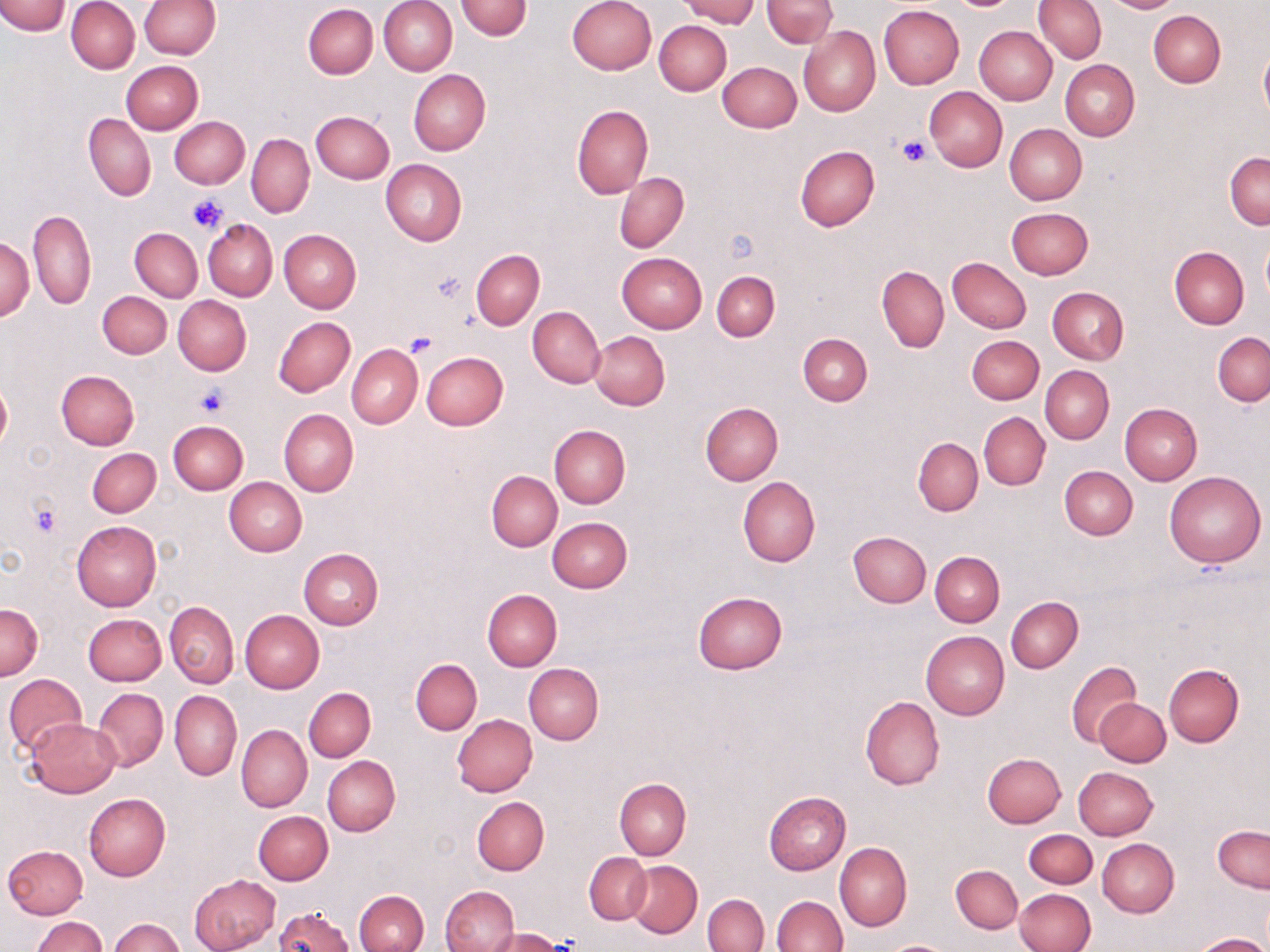
slide-level diagnosis = no evidence of blood parasites
stain = May-Grünwald-Giemsa
uninfected red blood cell locations = approximate bounding boxes as (x1, y1, x2, y2) in pixels: (67, 0, 139, 74), (138, 0, 219, 58), (380, 0, 457, 75), (567, 0, 656, 75), (680, 0, 758, 26), (761, 0, 837, 48), (1034, 0, 1107, 63), (1100, 0, 1183, 13), (0, 1, 70, 36), (456, 1, 532, 40), (303, 4, 378, 79), (878, 5, 964, 88), (1148, 11, 1225, 88), (654, 20, 731, 95), (974, 25, 1057, 104), (798, 26, 879, 116), (1259, 44, 1270, 122), (1060, 59, 1139, 141), (121, 61, 202, 135), (718, 61, 801, 133), (408, 69, 490, 155), (924, 86, 1007, 171), (573, 105, 653, 198), (311, 111, 394, 183), (83, 112, 156, 201), (170, 116, 249, 189), (1005, 123, 1087, 205), (247, 134, 315, 219), (795, 146, 879, 231), (1225, 151, 1270, 228), (380, 159, 467, 246), (615, 173, 689, 253), (1006, 207, 1093, 280), (28, 208, 97, 309), (203, 219, 278, 301), (130, 228, 202, 302), (279, 229, 361, 313), (1261, 236, 1270, 303), (1, 238, 34, 321), (1170, 246, 1249, 328), (472, 250, 544, 330), (616, 252, 708, 332), (947, 256, 1031, 333), (877, 265, 949, 353), (712, 271, 780, 341), (1047, 286, 1129, 364), (97, 291, 171, 358), (173, 296, 252, 376), (528, 306, 605, 387), (274, 316, 355, 398), (590, 331, 669, 410), (1213, 332, 1270, 406), (798, 333, 872, 406), (966, 335, 1044, 404), (347, 344, 422, 427), (421, 351, 508, 430), (1040, 366, 1114, 444), (56, 370, 139, 449), (0, 381, 11, 451), (701, 403, 782, 485), (1120, 403, 1203, 484), (279, 408, 358, 497), (978, 412, 1050, 490), (168, 419, 249, 494), (550, 426, 630, 507), (913, 437, 983, 516), (87, 448, 161, 518), (1060, 466, 1138, 540), (487, 471, 562, 551), (1163, 471, 1266, 568), (738, 476, 821, 567), (224, 477, 306, 556), (547, 517, 633, 592), (71, 521, 161, 611), (848, 531, 931, 607), (298, 549, 383, 630), (931, 552, 1004, 627), (481, 589, 561, 671), (693, 591, 787, 674), (1006, 597, 1082, 673), (164, 601, 238, 688), (0, 604, 43, 679), (240, 610, 324, 694), (83, 613, 165, 685), (921, 631, 1008, 720), (410, 658, 482, 734), (1067, 660, 1143, 748), (524, 662, 603, 744), (1164, 663, 1244, 747), (3, 673, 86, 755), (303, 687, 375, 762), (93, 688, 168, 771), (171, 689, 241, 780), (859, 696, 945, 790), (1095, 698, 1170, 767), (453, 715, 538, 796), (24, 718, 121, 797), (236, 724, 312, 812), (982, 752, 1066, 827), (323, 755, 399, 836), (1073, 767, 1158, 840), (615, 779, 691, 858), (764, 791, 850, 875), (85, 793, 171, 880), (472, 797, 549, 874), (253, 810, 333, 885), (1213, 826, 1269, 892), (1024, 829, 1097, 888), (1098, 839, 1179, 917), (835, 843, 912, 931), (2, 845, 88, 919), (584, 852, 651, 923), (626, 861, 702, 937), (950, 865, 1022, 933), (189, 874, 280, 952), (441, 886, 518, 952), (1014, 889, 1096, 952), (354, 890, 428, 952), (703, 894, 768, 952), (772, 896, 847, 952), (275, 906, 354, 952), (31, 915, 106, 952), (110, 918, 184, 952), (488, 928, 568, 952), (1194, 933, 1267, 952), (883, 941, 955, 952)
platelet locations = approximate bounding boxes as (x1, y1, x2, y2) in pixels: (898, 135, 935, 167), (187, 195, 227, 234), (431, 271, 467, 304), (407, 332, 437, 357), (194, 383, 228, 417), (30, 501, 61, 538)
modality = optical microscopy
magnification = 1000x
field of view = one of a larger specimen
preparation = thin blood film
image size = 1270×952 pixels